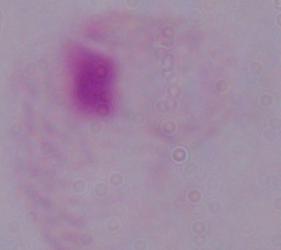
{
  "modality": "photomicrograph",
  "identification": "trichomonad",
  "magnification": "1000x"
}